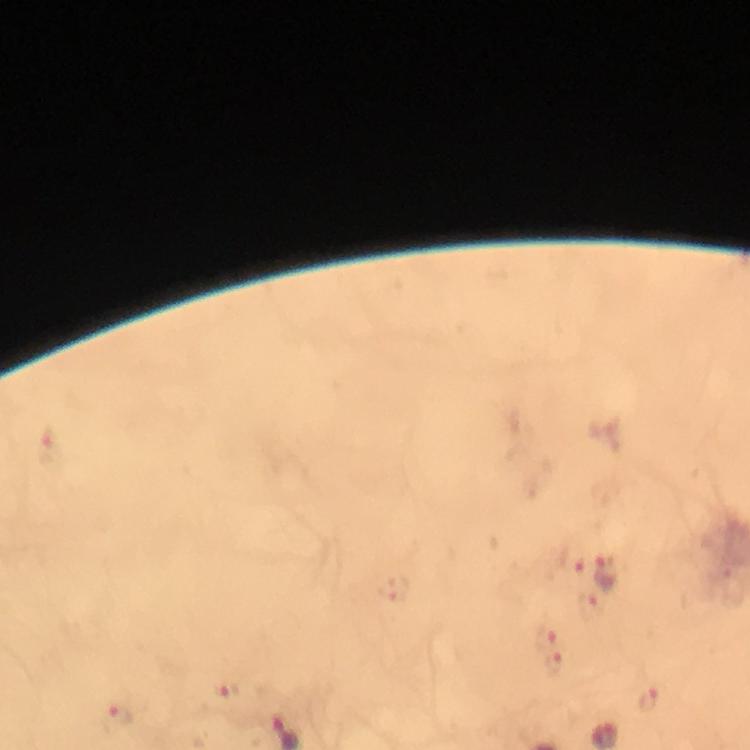

Approximate centers as (x, y) in pixels.
Summary:
  - Malaria parasite locations: (609, 572), (549, 635), (554, 664)
  - Immersion oil: applied
  - Preparation: thick blood smear
  - Stain: Giemsa
  - Image size: 750×750 pixels
  - Context: from a diagnostic examination for malaria
  - Cropped from: a single field of view
  - Magnification: 100x
  - Capture: smartphone camera through the microscope